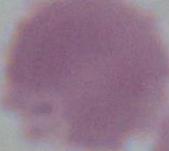
modality = micrograph
magnification = 1000x
identification = erythrocyte